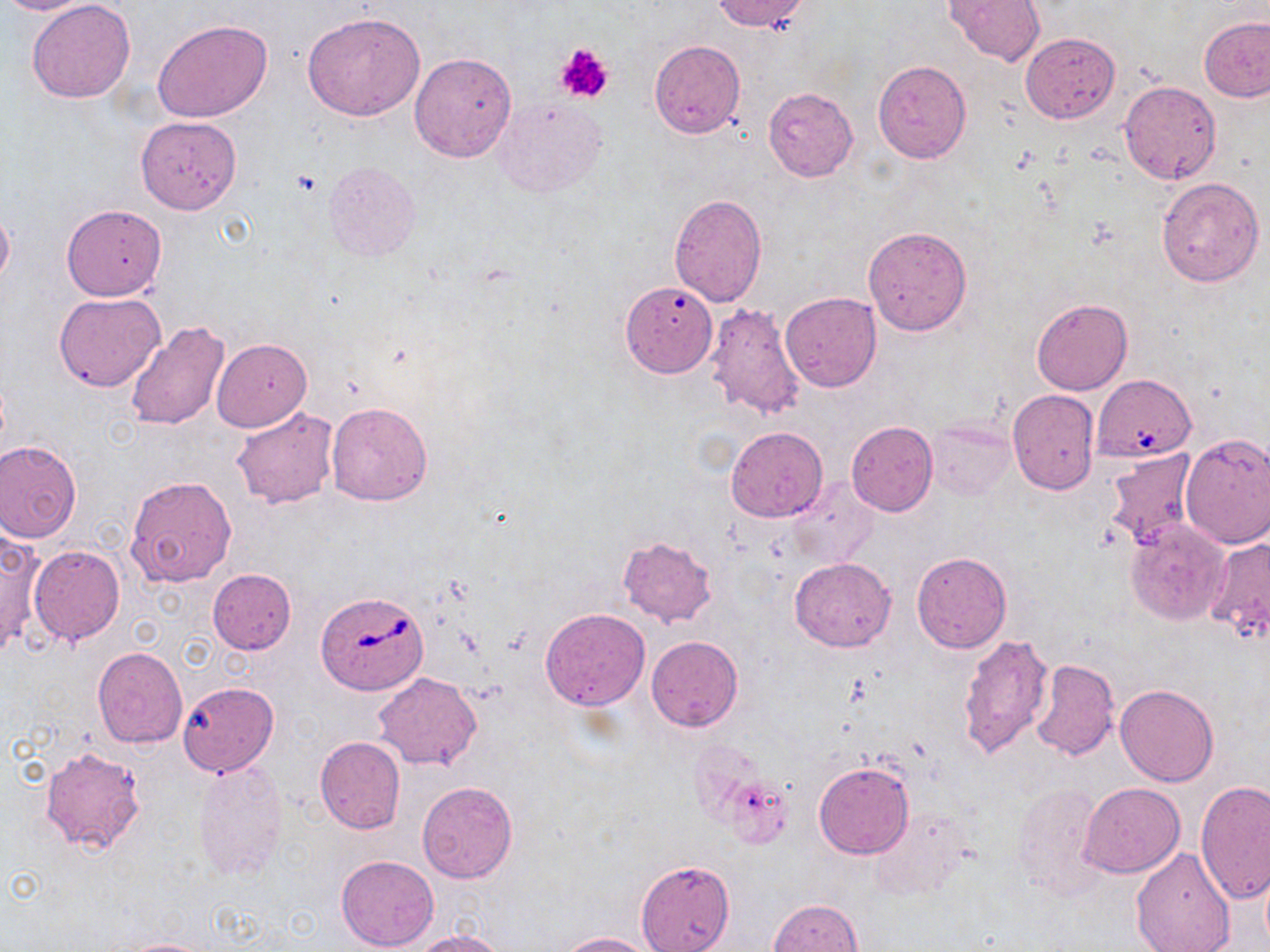

Approximate bounding boxes as (x1,y1)-(x2,y2) corner pairs in pixels. Uninfected red blood cell locations: (0,0)-(94,14), (27,0)-(137,103), (712,0)-(810,33), (945,0)-(1046,66), (302,10)-(425,121), (1199,15)-(1269,102), (152,18)-(274,122), (1019,32)-(1121,123), (649,41)-(745,140), (409,51)-(518,162), (873,60)-(971,163), (1118,80)-(1222,185), (762,87)-(859,182), (494,98)-(606,197), (135,115)-(243,215), (323,161)-(420,262), (1156,175)-(1265,287), (668,194)-(768,307), (0,203)-(14,292), (61,204)-(167,301), (862,225)-(972,336), (620,280)-(718,378), (54,293)-(165,393), (781,293)-(881,393), (1031,298)-(1133,395), (705,302)-(806,420), (126,319)-(232,430), (212,339)-(312,431), (1094,378)-(1197,461), (1008,390)-(1099,492), (325,401)-(433,506), (230,406)-(338,509), (926,419)-(1015,500), (846,422)-(937,516), (726,427)-(828,521), (1180,433)-(1270,548), (0,439)-(83,542), (1104,448)-(1199,547), (125,475)-(237,587), (786,477)-(876,567), (1124,519)-(1229,625), (0,527)-(43,656), (616,536)-(717,627), (1204,536)-(1270,644), (28,545)-(124,645), (911,550)-(1012,653), (790,557)-(896,650), (207,569)-(296,654), (540,609)-(650,711), (959,634)-(1053,759), (646,635)-(743,731), (93,647)-(187,748), (1029,658)-(1120,761), (374,673)-(481,770), (179,681)-(279,776), (1115,684)-(1219,786), (315,737)-(405,834), (40,745)-(146,856), (812,760)-(914,859), (191,763)-(289,884), (720,776)-(793,849), (1196,780)-(1269,906), (417,782)-(517,883), (1010,782)-(1105,898), (1082,782)-(1185,877), (870,805)-(973,901), (1130,844)-(1236,951), (336,855)-(438,951), (636,858)-(734,952), (769,898)-(863,952), (413,929)-(506,952), (559,931)-(657,952), (117,938)-(220,952). Babesia divergens-infected red blood cell locations: (318,591)-(427,693). Platelet locations: (554,42)-(614,105). Slide-level diagnosis: Babesia divergens. May-Grünwald-Giemsa stain. Image is 1270×952 pixels. Captured at 1000x magnification. Thin blood smear. Light microscopy. Single field of view.